Point out each Plasmodium parasite.
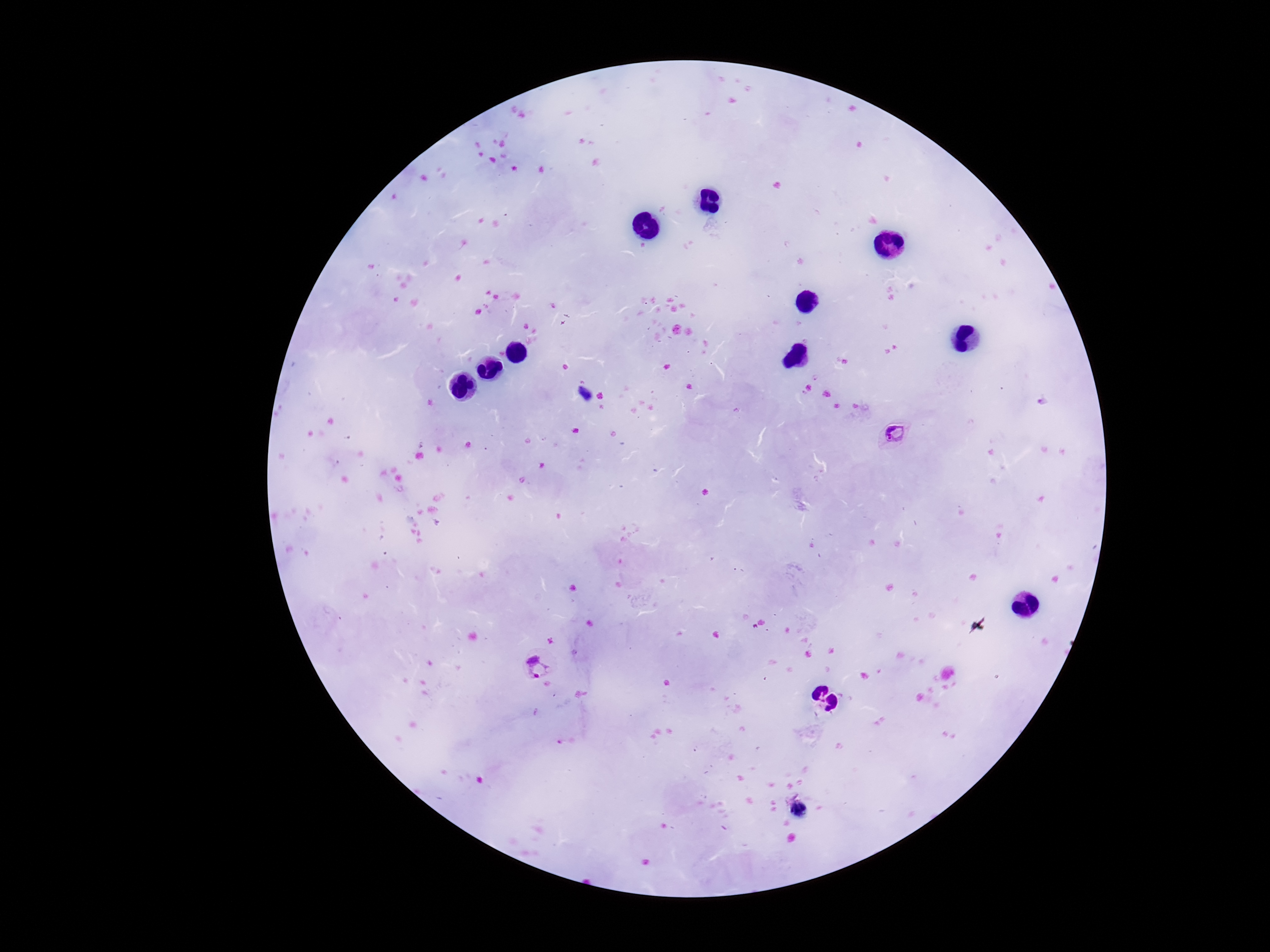

Approximate centers as (x, y) in pixels.
Plasmodium parasites: (897, 435), (538, 667).

Summary:
  - Field of view: one from this slide
  - Preparation: thick peripheral-blood smear
  - Patient malaria status: positive
  - Magnification: 100x
  - Capture: smartphone camera through the microscope eyepiece
  - Image size: 1270×952 pixels
  - Stain: Giemsa